Report the malaria status of this cell.
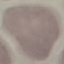

Uninfected.

Acquired by smartphone through the microscope eyepiece. Giemsa-stained preparation. Thin smear of blood. Automatically extracted cell patch, resized to 64 × 64 pixels.